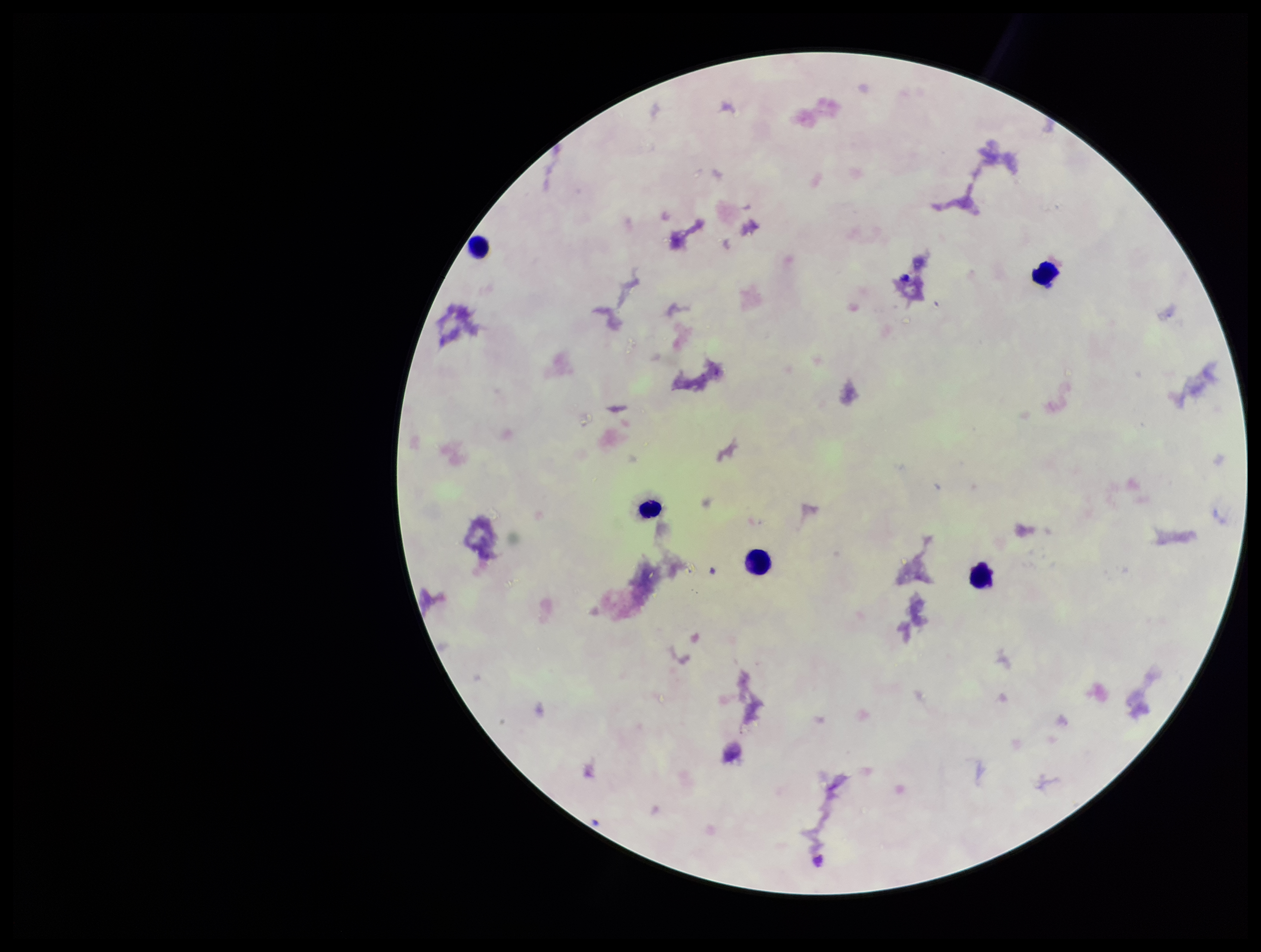

Preparation: thick blood smear. Stained with Giemsa. Smartphone photograph taken through the eyepiece of a microscope. One field from this slide. Parasite count: 0. Image is 1261×952 pixels. Patient malaria status: negative. Plasmodium parasites: none identified. Leukocyte count: 5.